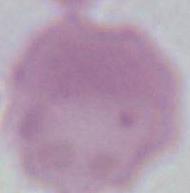
Summary:
  - Modality: photomicrograph
  - Identification: red blood cell
  - Magnification: 1000x